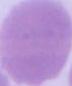
A red blood cell is shown. 1000x magnification. Micrograph.